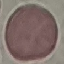
Summary:
  - Result: negative for malaria parasites
  - Stain: Giemsa
  - Capture: smartphone through the microscope eyepiece
  - Preparation: thin blood film
  - Image type: cell patch, automatically extracted from a larger field of view and resized to 64 × 64 pixels